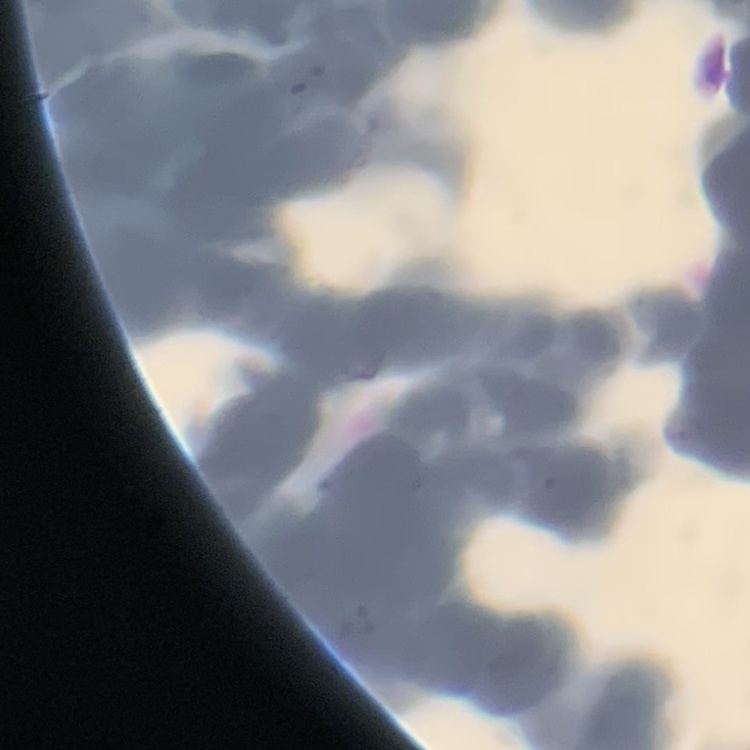

{
  "red_blood_cell_morphology": "rouleaux formation",
  "preparation": "thin peripheral smear",
  "image_type": "square crop of a larger photomicrograph",
  "stain": "Field's or Giemsa"
}